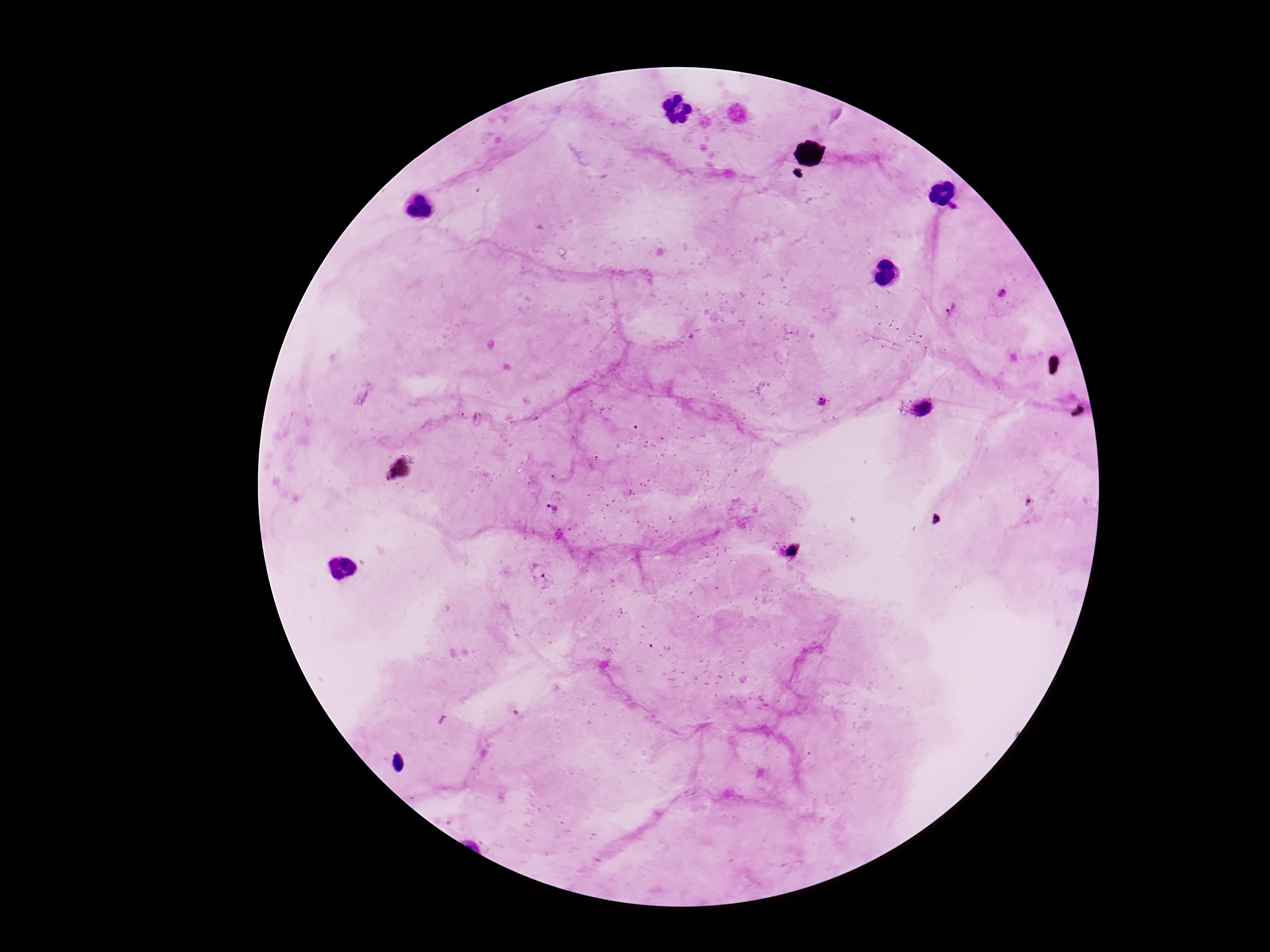

Approximate centers as (x, y) in pixels.
Summary:
  - Plasmodium parasite locations: (954, 207), (1002, 293), (950, 309), (823, 402), (923, 408), (552, 508), (791, 552), (540, 569)
  - Preparation: thick peripheral-blood smear
  - Magnification: 100x
  - Capture: smartphone camera through the microscope eyepiece
  - Patient malaria status: infected
  - Field of view: one from this slide
  - Stain: Giemsa
  - Image size: 1270×952 pixels